Give the extent of all Plasmodium ovale-infected red blood cells.
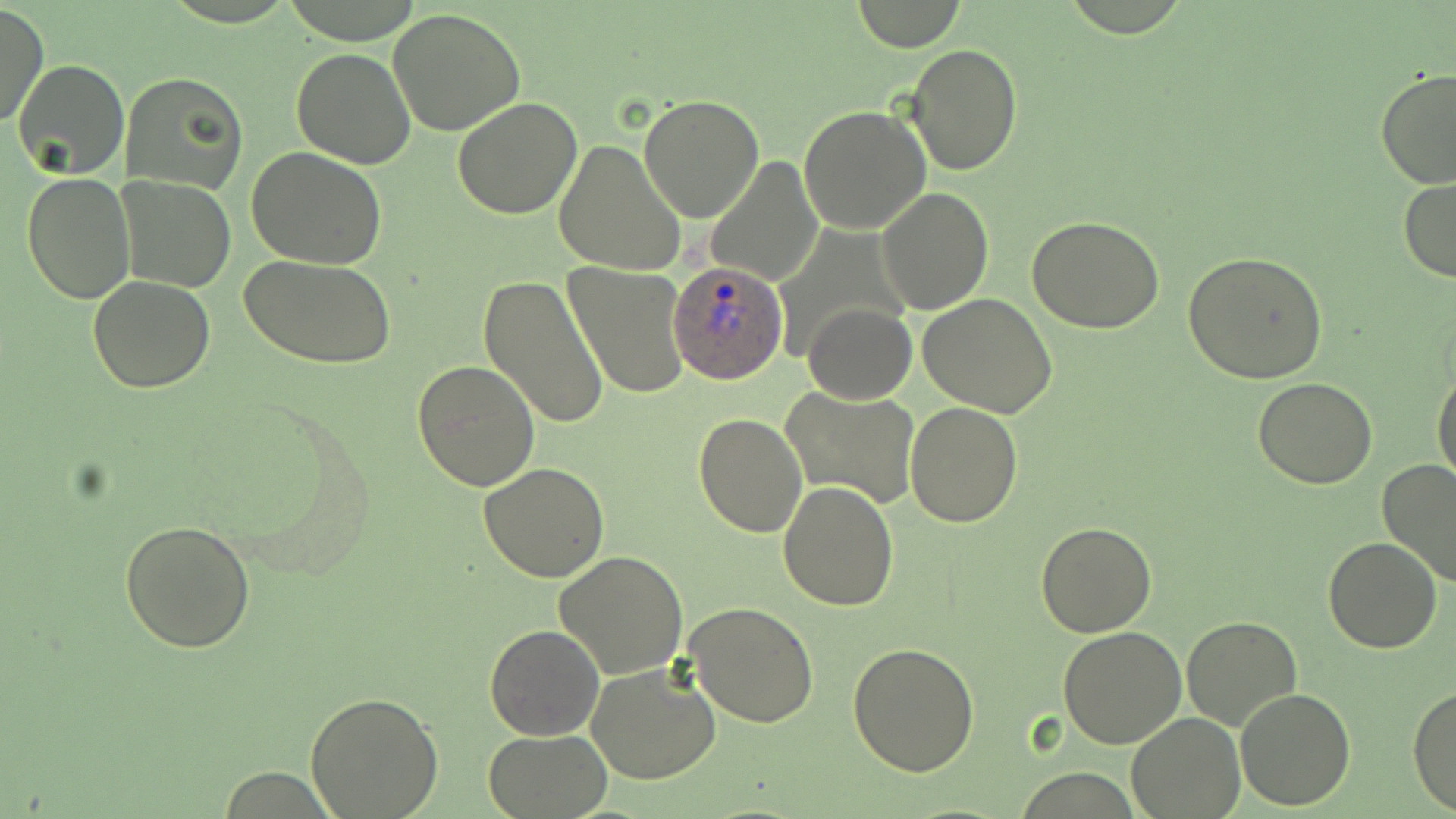

Approximate bounding boxes as named x1/y1/x2/y2 corners in pixels.
Plasmodium ovale-infected red blood cells: (x1=667, y1=261, x2=788, y2=386).

Uninfected red blood cell locations: (x1=850, y1=1, x2=966, y2=50), (x1=0, y1=4, x2=49, y2=130), (x1=390, y1=8, x2=527, y2=135), (x1=905, y1=44, x2=1024, y2=177), (x1=291, y1=47, x2=416, y2=169), (x1=11, y1=58, x2=129, y2=180), (x1=1376, y1=69, x2=1455, y2=191), (x1=120, y1=70, x2=249, y2=195), (x1=639, y1=95, x2=765, y2=223), (x1=452, y1=98, x2=584, y2=221), (x1=798, y1=103, x2=931, y2=233), (x1=553, y1=140, x2=687, y2=276), (x1=246, y1=147, x2=387, y2=270), (x1=704, y1=154, x2=822, y2=286), (x1=22, y1=171, x2=134, y2=303), (x1=1397, y1=176, x2=1456, y2=282), (x1=118, y1=177, x2=236, y2=292), (x1=876, y1=187, x2=994, y2=315), (x1=1027, y1=216, x2=1168, y2=333), (x1=1183, y1=251, x2=1328, y2=384), (x1=241, y1=254, x2=397, y2=370), (x1=563, y1=263, x2=690, y2=400), (x1=477, y1=273, x2=610, y2=431), (x1=88, y1=274, x2=217, y2=392), (x1=918, y1=293, x2=1059, y2=417), (x1=801, y1=303, x2=916, y2=405), (x1=435, y1=311, x2=594, y2=477), (x1=412, y1=360, x2=541, y2=492), (x1=1432, y1=368, x2=1456, y2=486), (x1=1253, y1=378, x2=1377, y2=489), (x1=779, y1=386, x2=921, y2=512), (x1=905, y1=402, x2=1023, y2=529), (x1=693, y1=411, x2=809, y2=537), (x1=1375, y1=458, x2=1456, y2=589), (x1=478, y1=462, x2=611, y2=583), (x1=779, y1=480, x2=898, y2=612), (x1=120, y1=519, x2=257, y2=653), (x1=1036, y1=522, x2=1155, y2=637), (x1=1322, y1=537, x2=1443, y2=654), (x1=554, y1=552, x2=689, y2=679), (x1=685, y1=601, x2=818, y2=728), (x1=1181, y1=614, x2=1304, y2=733), (x1=484, y1=624, x2=604, y2=741), (x1=1058, y1=627, x2=1188, y2=748), (x1=848, y1=641, x2=982, y2=776), (x1=586, y1=663, x2=722, y2=785), (x1=1409, y1=686, x2=1456, y2=814), (x1=1234, y1=688, x2=1358, y2=810), (x1=305, y1=691, x2=443, y2=817), (x1=1127, y1=712, x2=1245, y2=818), (x1=483, y1=730, x2=612, y2=818). Slide-level diagnosis: Plasmodium ovale. May-Grünwald-Giemsa-stained preparation. Thin blood film. 1000x magnification. Image is 1456×819 pixels. Optical microscopy. One field of a larger specimen.